Identify the blood parasite species.
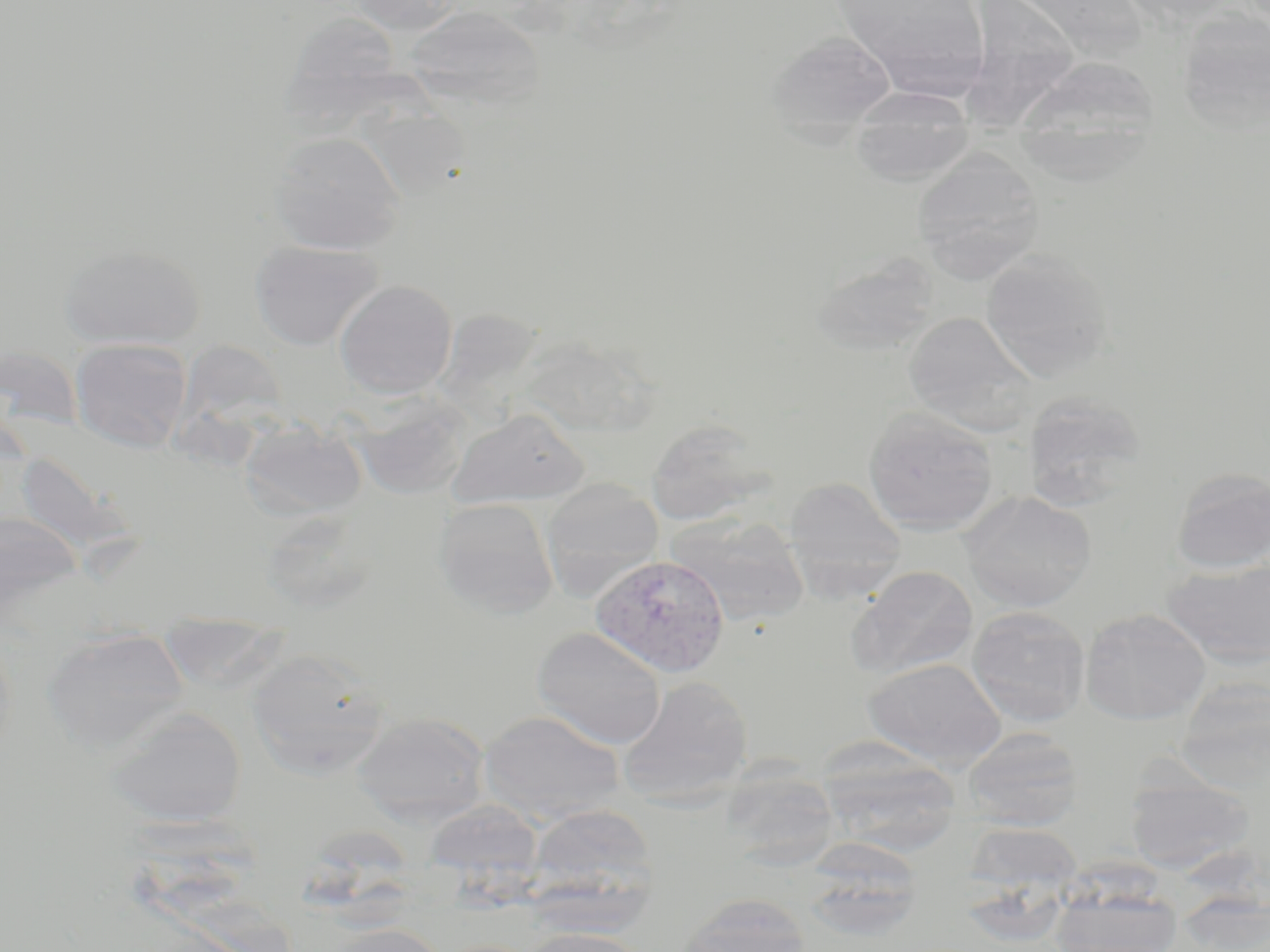
Plasmodium vivax.

Approximate bounding boxes as [x1, y1, x2, y2] in pixels. Uninfected red blood cell locations: [346, 0, 464, 34], [831, 0, 992, 97], [1117, 0, 1240, 31], [967, 2, 1082, 140], [404, 6, 546, 113], [1176, 9, 1270, 137], [291, 18, 428, 141], [766, 31, 897, 139], [1012, 54, 1162, 178], [849, 86, 975, 185], [361, 104, 469, 198], [268, 131, 406, 255], [912, 149, 1045, 282], [250, 239, 384, 351], [57, 244, 206, 350], [980, 249, 1113, 382], [810, 253, 941, 358], [335, 279, 457, 399], [903, 311, 1040, 435], [69, 337, 193, 453], [1022, 392, 1147, 509], [347, 393, 470, 500], [863, 407, 999, 536], [449, 408, 588, 509], [239, 418, 368, 522], [645, 418, 774, 527], [1170, 467, 1270, 574], [783, 477, 906, 599], [540, 478, 664, 601], [960, 490, 1096, 612], [434, 497, 559, 618], [0, 510, 86, 623], [666, 514, 810, 628], [1163, 557, 1270, 670], [846, 565, 978, 682], [966, 606, 1090, 728], [1081, 608, 1211, 725], [41, 627, 189, 752], [531, 627, 667, 749], [246, 648, 390, 778], [863, 657, 1006, 770], [617, 675, 753, 804], [1176, 678, 1270, 794], [106, 706, 247, 829], [480, 709, 625, 824], [351, 712, 490, 826], [962, 727, 1085, 830], [817, 746, 960, 857], [719, 765, 841, 871], [1125, 771, 1254, 874], [525, 803, 658, 912], [963, 822, 1084, 898], [799, 839, 926, 941], [1049, 880, 1184, 952], [676, 893, 813, 952], [1176, 894, 1270, 951], [320, 923, 450, 952], [518, 926, 652, 952]. Plasmodium vivax-infected red blood cell locations: [591, 553, 730, 677]. Light microscopy. 1000x magnification. Thin blood smear. Single field of view. May-Grünwald-Giemsa stain. Image is 1270×952 pixels.